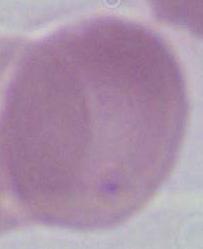

Summary:
  - Identification: red blood cell
  - Modality: photomicrograph
  - Magnification: 1000x